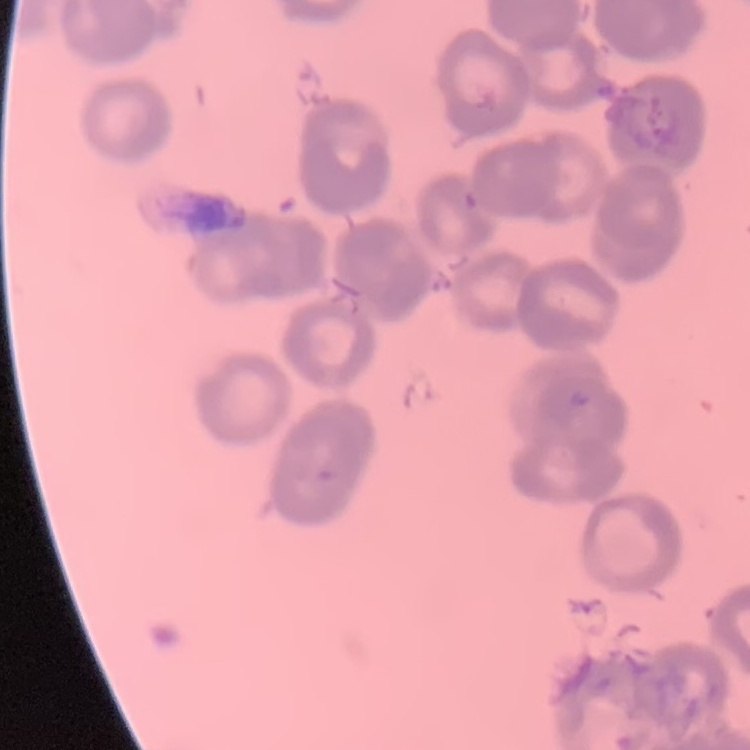
erythrocyte morphology = rouleaux formation
image type = square crop of a larger photomicrograph
stain = Field's or Giemsa
preparation = thin peripheral smear